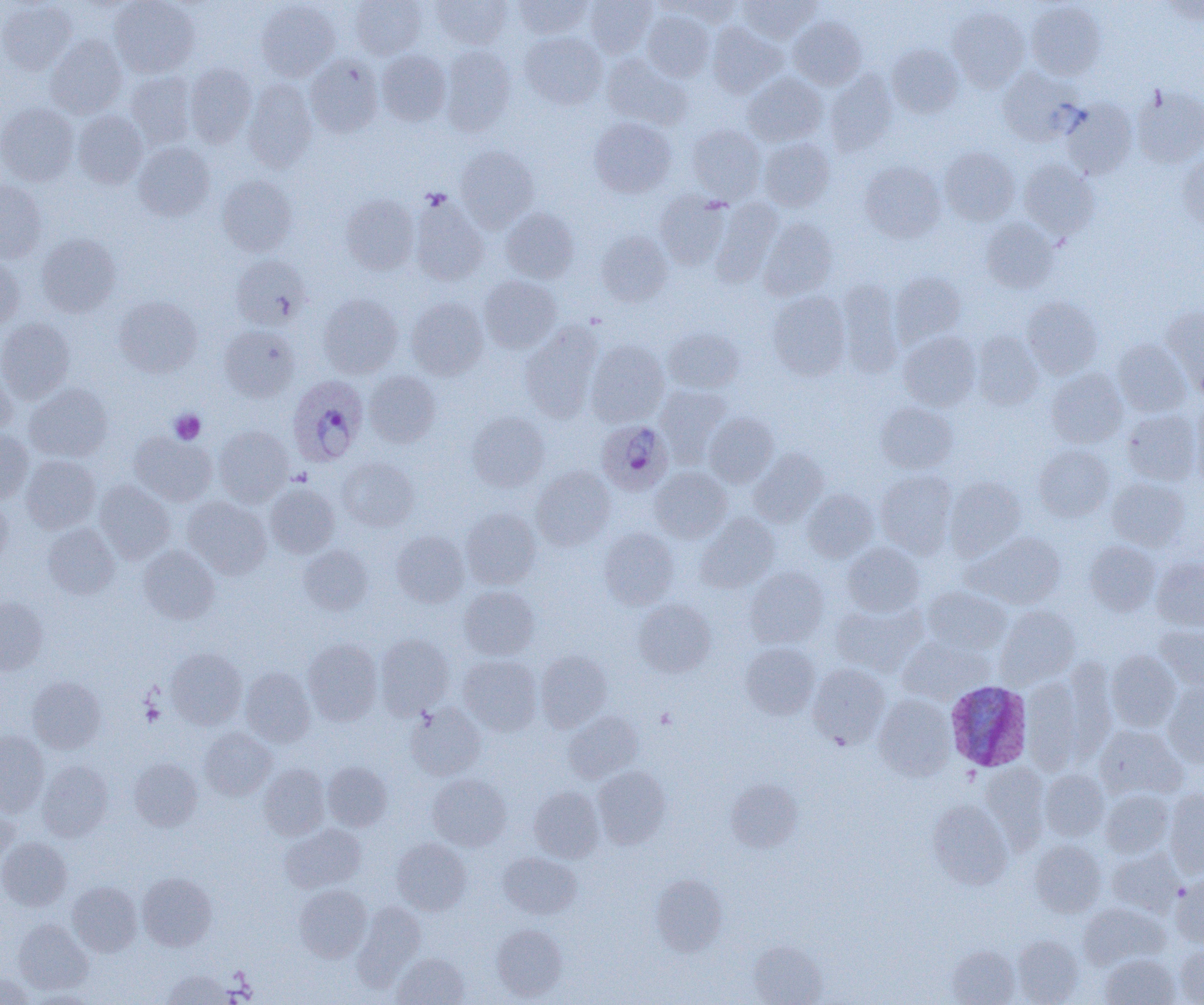

Approximate bounding boxes as (x1,y1)-(x2,y2) corner pairs in pixels. Uninfected red blood cell locations: (0,0)-(77,75), (110,0)-(199,77), (350,0)-(427,60), (432,0)-(512,49), (513,0)-(592,38), (584,0)-(658,58), (738,0)-(819,43), (257,1)-(340,81), (669,1)-(746,26), (1026,1)-(1106,80), (1161,1)-(1203,25), (947,5)-(1029,92), (642,10)-(714,82), (789,17)-(866,89), (708,23)-(785,96), (520,31)-(607,109), (46,35)-(127,118), (887,44)-(964,118), (440,45)-(516,136), (377,50)-(451,125), (602,54)-(691,129), (305,55)-(383,137), (184,63)-(256,146), (997,67)-(1080,143), (825,70)-(897,155), (125,72)-(197,148), (743,73)-(827,146), (243,79)-(317,171), (1131,85)-(1204,168), (1061,100)-(1137,179), (0,103)-(78,186), (72,111)-(147,188), (589,118)-(677,197), (686,124)-(766,203), (759,137)-(834,211), (133,142)-(214,221), (455,146)-(538,230), (939,147)-(1019,225), (1178,155)-(1204,233), (1019,159)-(1099,239), (860,162)-(945,242), (216,175)-(297,256), (0,179)-(47,263), (654,192)-(732,269), (340,194)-(419,275), (410,196)-(489,285), (711,199)-(782,285), (501,208)-(579,283), (759,218)-(838,300), (981,218)-(1058,293), (596,230)-(672,306), (36,234)-(121,317), (0,254)-(24,330), (231,255)-(309,330), (890,272)-(966,348), (479,276)-(561,352), (837,280)-(904,377), (768,291)-(851,380), (319,294)-(402,377), (114,296)-(202,377), (1022,296)-(1103,378), (406,297)-(488,379), (1163,308)-(1204,397), (0,317)-(76,402), (520,324)-(603,421), (219,325)-(299,400), (664,327)-(743,393), (899,331)-(981,411), (971,331)-(1044,410), (1113,339)-(1190,416), (586,340)-(669,425), (1046,368)-(1127,448), (0,369)-(17,437), (365,371)-(441,447), (25,382)-(113,462), (656,385)-(733,465), (875,402)-(958,473), (1190,404)-(1204,488), (1122,409)-(1201,485), (467,412)-(550,491), (704,412)-(779,487), (212,426)-(293,505), (0,429)-(33,503), (130,432)-(215,505), (1033,444)-(1114,521), (749,449)-(828,527), (21,455)-(100,533), (338,457)-(419,531), (531,466)-(615,549), (650,467)-(731,542), (876,469)-(957,557), (945,477)-(1025,559), (1107,477)-(1189,550), (95,481)-(175,563), (265,483)-(339,558), (802,489)-(878,562), (183,497)-(272,579), (0,498)-(12,571), (461,508)-(541,589), (696,513)-(779,592), (42,524)-(119,599), (599,528)-(679,609), (391,530)-(469,607), (966,532)-(1066,609), (1085,541)-(1160,616), (843,542)-(924,617), (139,545)-(219,624), (299,545)-(373,615), (1152,556)-(1204,631), (746,568)-(828,648), (460,586)-(539,660), (921,586)-(1010,655), (0,596)-(48,674), (633,599)-(716,677), (831,601)-(926,675), (996,605)-(1080,687), (1155,624)-(1204,688), (375,633)-(454,718), (898,634)-(993,704), (303,639)-(382,725), (740,642)-(820,719), (166,648)-(246,729), (1106,650)-(1181,732), (535,651)-(612,731), (458,655)-(542,735), (1060,659)-(1118,761), (807,663)-(890,748), (240,667)-(315,746), (28,676)-(105,753), (1023,677)-(1083,773), (1163,680)-(1204,767), (874,694)-(956,780), (406,703)-(486,779), (564,711)-(643,783), (1095,725)-(1187,800), (200,727)-(276,800), (0,731)-(49,815), (129,758)-(202,831), (37,761)-(113,841), (322,761)-(392,831), (980,762)-(1050,851), (259,765)-(329,840), (593,766)-(671,848), (1039,769)-(1109,841), (427,773)-(511,850), (726,779)-(802,852), (529,786)-(605,862), (1100,789)-(1174,857), (1164,790)-(1204,876), (927,799)-(1012,888), (0,802)-(18,865), (280,824)-(365,892), (0,837)-(71,910), (392,838)-(472,915), (1030,840)-(1106,917), (1107,848)-(1183,916), (498,852)-(580,919), (138,872)-(216,951), (651,873)-(728,956), (1171,875)-(1204,946), (68,881)-(142,956), (294,885)-(371,962), (354,901)-(425,986), (1079,902)-(1169,969), (14,919)-(92,994), (491,924)-(567,1000), (1012,935)-(1083,1004), (748,939)-(827,1005), (1175,944)-(1204,1005), (946,945)-(1020,1005), (393,953)-(469,1005), (1100,953)-(1180,1005), (161,970)-(236,1005), (0,973)-(35,1004). Plasmodium ovale-infected red blood cell locations: (287,376)-(368,467), (602,422)-(670,496), (945,680)-(1033,772). Platelet locations: (169,410)-(206,444), (141,701)-(164,726), (656,708)-(676,728). Slide-level diagnosis: Plasmodium ovale. Image is 1204×1005 pixels. Light microscopy. Thin blood smear. Single field of view. Captured at 1000x magnification.